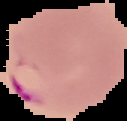
Summary:
  - Preparation: thin blood film
  - Result: malaria parasites detected
  - Image type: segmented cell region on a black background
  - Image size: 127×121 pixels